Give the preparation type.
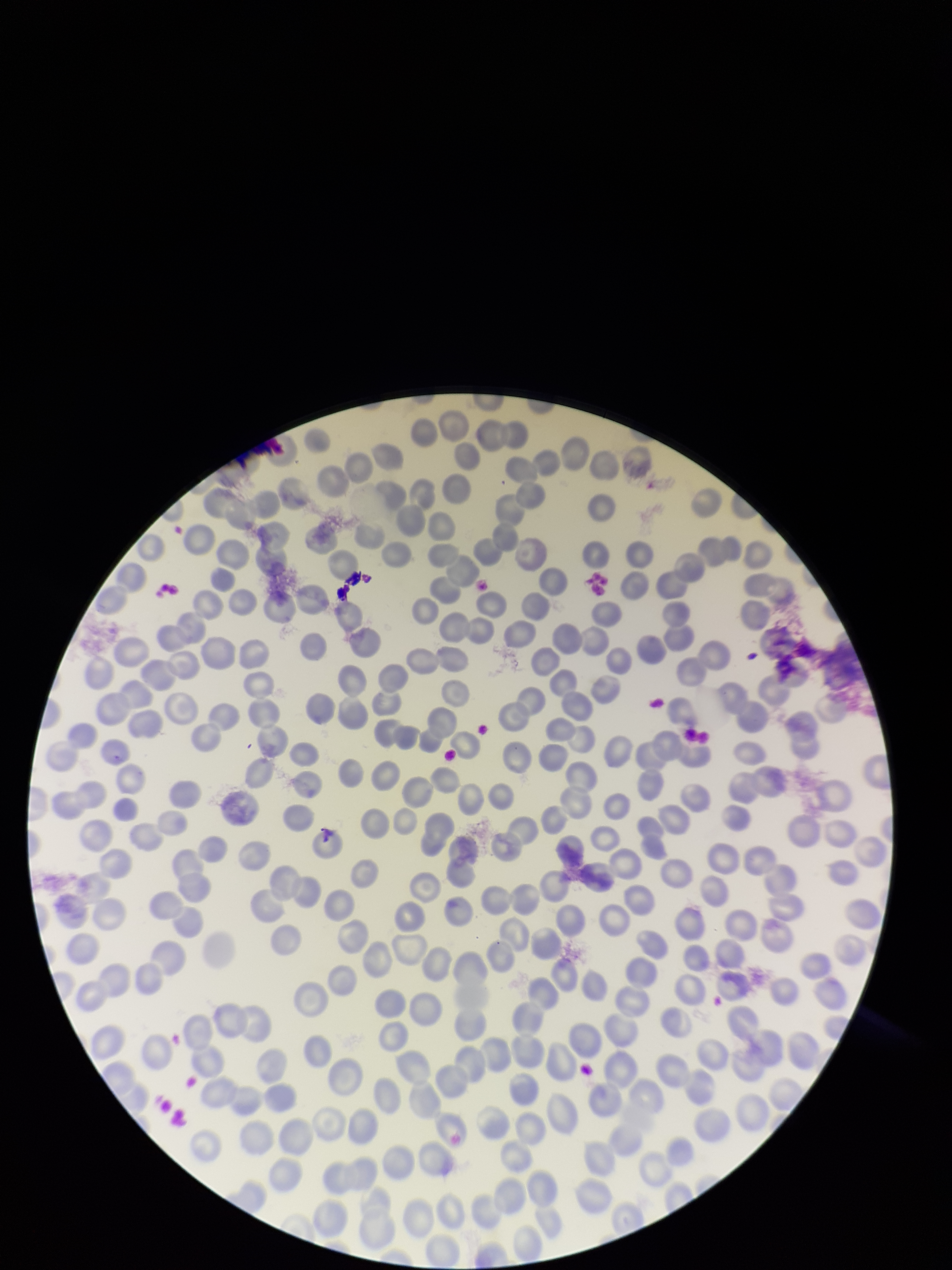

Thin.

Summary:
  - Field of view: one from this slide
  - Image size: 952×1270 pixels
  - Red blood cell count: 235
  - Patient malaria status: negative
  - Capture: smartphone photograph through the microscope eyepiece
  - Stain: Giemsa
  - Parasitized red blood cell count: 0
  - Parasitized red blood cells: none seen